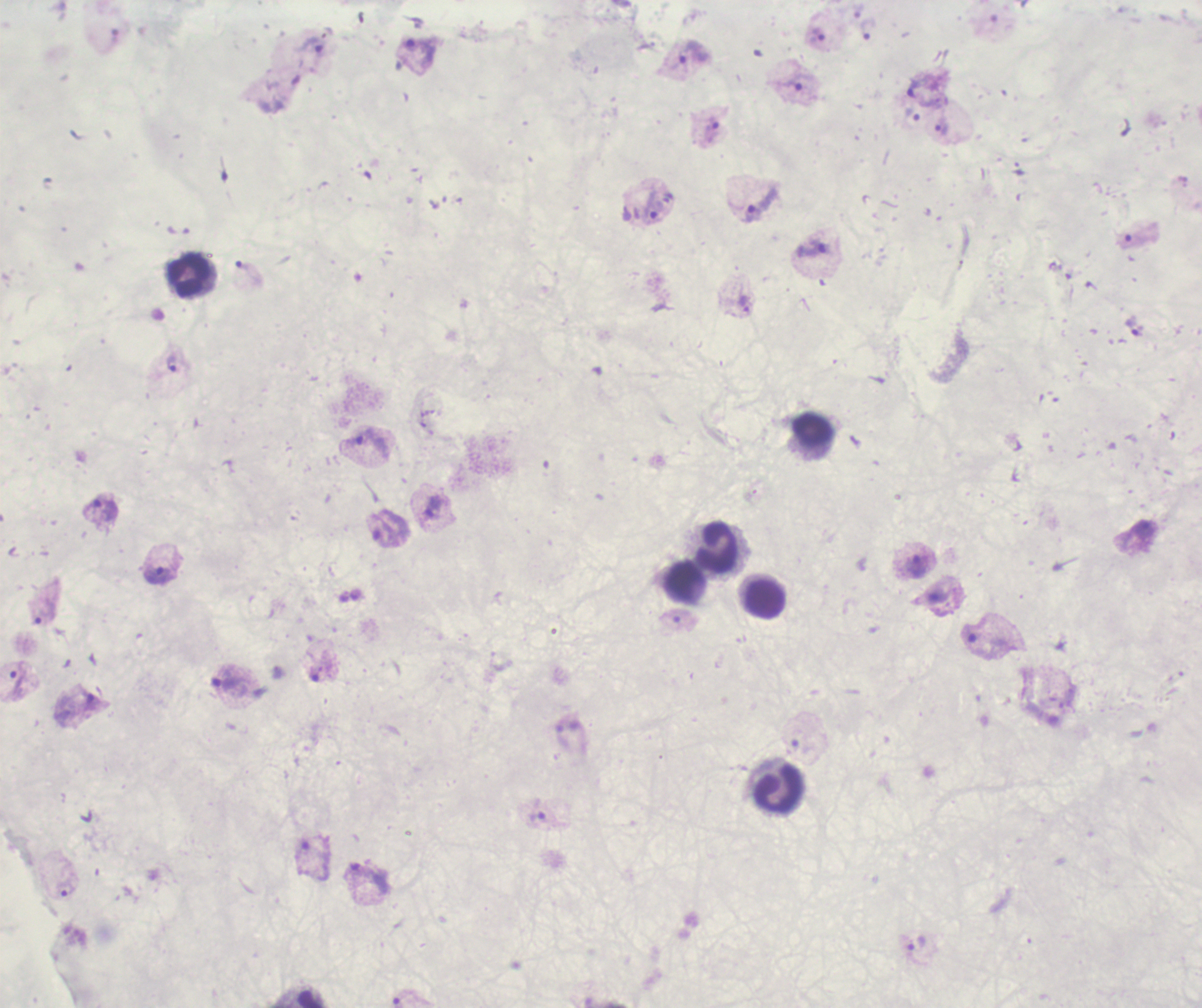 Approximate centers as {x, y} in pixels. Leukocyte locations: {189, 277}, {812, 428}, {713, 547}, {685, 582}, {764, 598}, {777, 790}, {309, 997}. Trophozoite locations: {858, 11}, {868, 29}, {815, 35}, {311, 46}, {693, 51}, {418, 53}, {793, 84}, {914, 87}, {912, 115}, {942, 127}, {712, 130}, {761, 204}, {653, 205}, {1137, 240}, {815, 248}, {247, 272}, {745, 305}, {1137, 328}, {173, 364}, {368, 443}, {432, 505}, {104, 510}, {380, 529}, {1143, 532}, {916, 566}, {159, 574}, {938, 597}, {43, 612}, {974, 635}, {320, 666}, {227, 680}, {18, 682}, {91, 705}, {538, 815}, {303, 855}, {368, 876}, {65, 889}, {915, 942}. Result: Plasmodium parasites identified. Romanowsky-stained preparation. Thick smear of blood. Previously used in an actual diagnosis. Background quality: unsatisfactory. 100x magnification. Image is 1202×1008 pixels. Single field of view.